Classify this cell by malaria status.
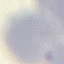
Uninfected.

Summary:
  - Image type: automatically extracted cell patch, resized to 64 × 64 pixels
  - Capture: smartphone camera at the microscope eyepiece
  - Stain: Giemsa
  - Preparation: thin blood film